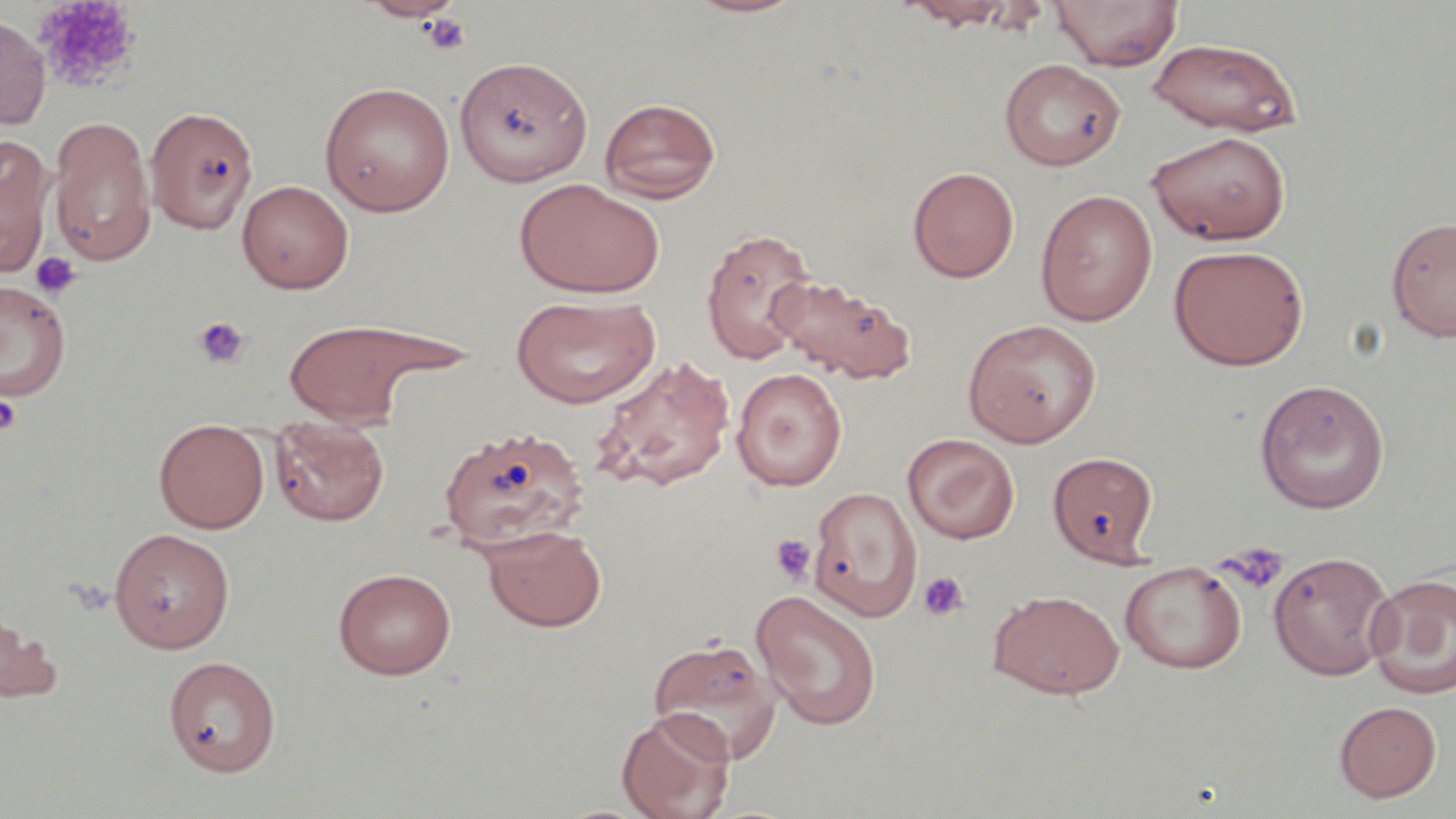

Summary:
  - Coordinate format: approximate bounding boxes as (x1, y1, x2, y2) in pixels
  - Platelet locations: (34, 0, 141, 93), (421, 12, 471, 55), (29, 251, 82, 299), (192, 316, 250, 369), (0, 393, 22, 435), (769, 534, 817, 586), (1218, 542, 1289, 593), (918, 571, 969, 622)
  - Uninfected red blood cell locations: (359, 0, 464, 22), (682, 0, 809, 18), (1050, 0, 1182, 71), (902, 1, 1017, 30), (0, 14, 50, 130), (1146, 38, 1303, 136), (454, 55, 593, 186), (999, 58, 1125, 171), (319, 82, 455, 216), (599, 96, 721, 202), (145, 106, 259, 234), (49, 118, 155, 266), (1145, 130, 1291, 245), (0, 137, 54, 275), (907, 166, 1019, 283), (515, 178, 666, 299), (237, 179, 354, 293), (1035, 189, 1158, 327), (1386, 216, 1456, 342), (700, 227, 818, 365), (1168, 244, 1308, 370), (769, 274, 915, 384), (0, 279, 72, 403), (511, 295, 660, 408), (962, 318, 1101, 447), (283, 319, 440, 425), (589, 355, 736, 493), (731, 368, 847, 491), (1254, 378, 1390, 514), (270, 417, 389, 526), (155, 419, 269, 533), (438, 425, 588, 556), (903, 433, 1020, 544), (1048, 451, 1158, 566), (808, 486, 922, 622), (480, 524, 607, 632), (109, 528, 235, 653), (1268, 550, 1396, 680), (1119, 560, 1247, 673), (333, 568, 456, 679), (1365, 572, 1456, 700), (751, 589, 882, 730), (988, 589, 1124, 699), (0, 607, 62, 705), (648, 637, 783, 763), (163, 656, 280, 776), (1334, 700, 1442, 802), (616, 707, 736, 819)
  - Slide-level diagnosis: no evidence of blood parasites
  - Field of view: one of a larger specimen
  - Magnification: 1000x
  - Modality: optical microscopy
  - Image size: 1456×819 pixels
  - Stain: May-Grünwald-Giemsa
  - Preparation: thin blood smear